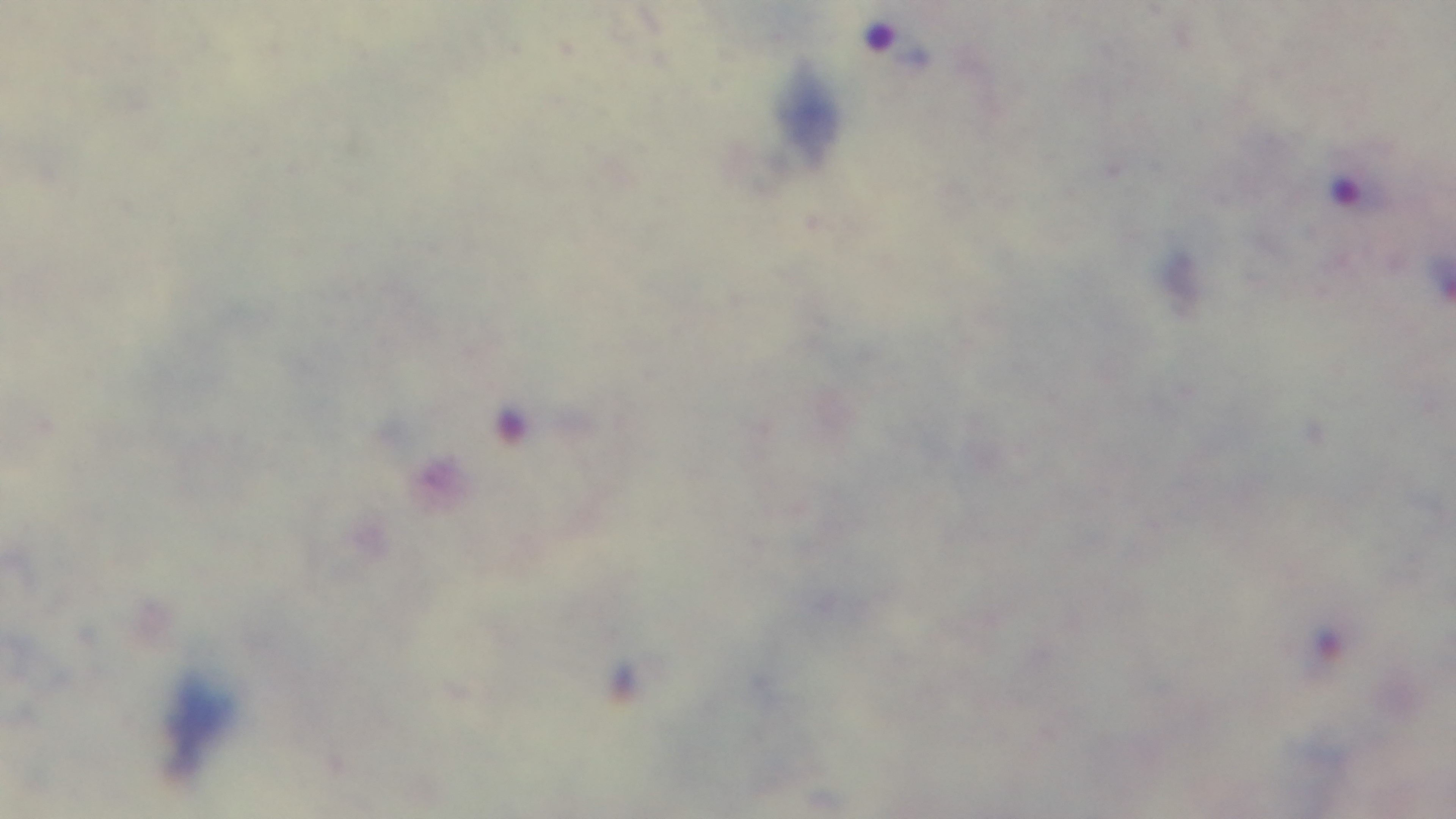

Single field of view. Preparation: thick smear. Captured with a mounted 4K digital camera. 100x oil-immersion objective. Giemsa-stained. Photomicrograph. Malaria status: positive.